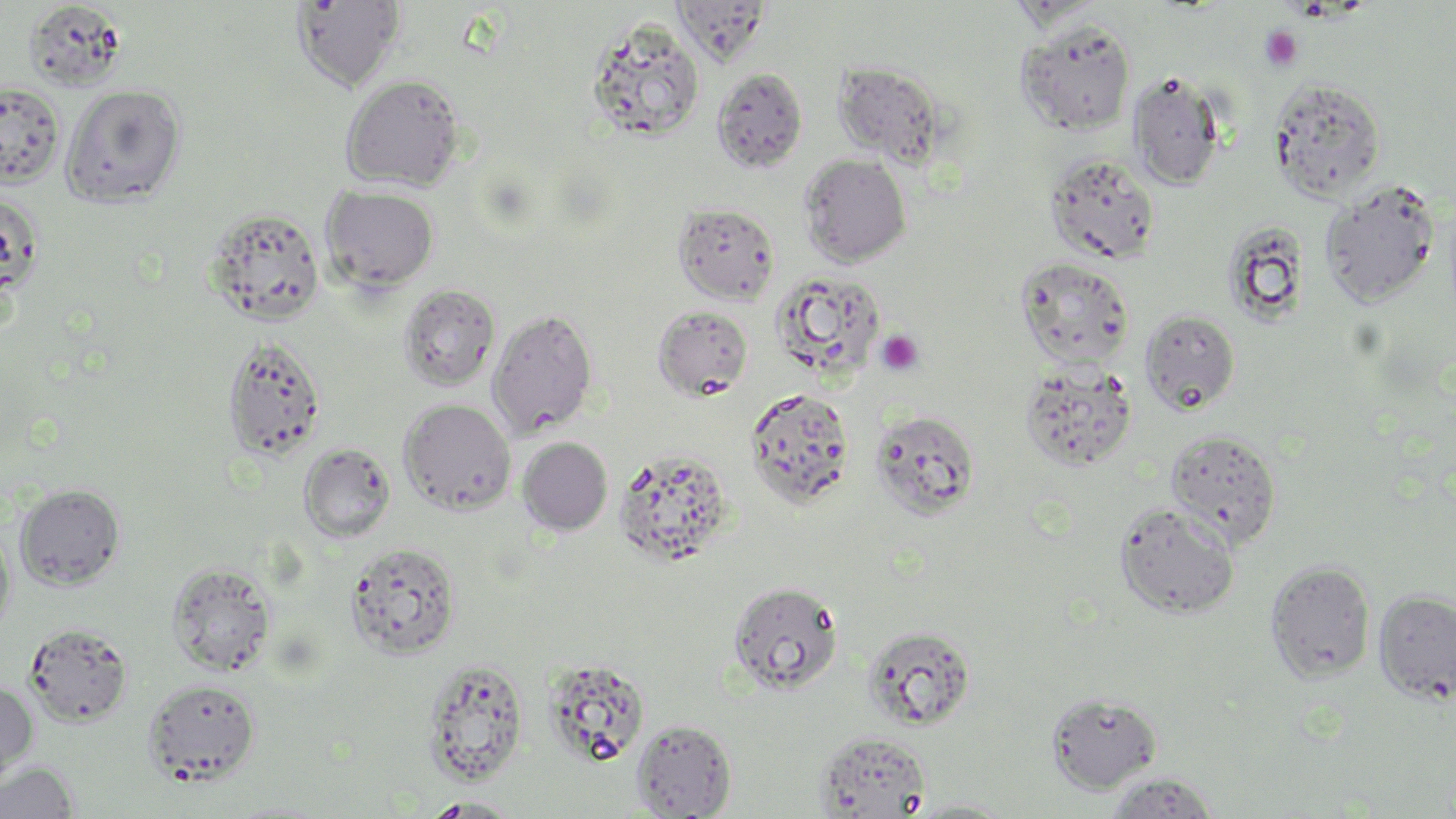
Summary:
  - Coordinate format: approximate bounding boxes as (x1,y1)-(x2,y2) corner pairs in pixels
  - Platelet locations: (1259,25)-(1304,72), (876,329)-(925,376)
  - Uninfected red blood cell locations: (290,0)-(407,93), (672,1)-(771,65), (24,2)-(127,92), (586,18)-(706,142), (1015,18)-(1136,136), (833,62)-(946,166), (711,68)-(807,174), (1128,71)-(1226,190), (340,74)-(466,191), (1269,78)-(1386,202), (0,81)-(65,188), (60,84)-(186,208), (1044,152)-(1160,265), (798,153)-(912,267), (1320,181)-(1440,309), (321,185)-(439,292), (0,191)-(44,304), (672,203)-(780,305), (204,207)-(326,327), (1221,220)-(1311,327), (1015,257)-(1135,370), (770,270)-(887,381), (397,284)-(501,392), (652,305)-(754,401), (487,307)-(598,439), (1139,309)-(1241,416), (222,335)-(327,463), (1020,363)-(1137,472), (745,387)-(854,507), (398,399)-(517,515), (869,409)-(980,520), (1165,429)-(1282,547), (517,437)-(612,535), (298,443)-(396,543), (614,447)-(736,569), (15,484)-(125,590), (1114,501)-(1241,618), (0,522)-(16,642), (346,541)-(462,659), (1265,560)-(1377,683), (167,561)-(277,677), (728,581)-(843,695), (1374,589)-(1456,705), (25,621)-(132,726), (862,625)-(977,730), (542,657)-(650,767), (422,658)-(528,786), (142,678)-(261,786), (0,680)-(37,785), (1045,692)-(1163,793), (631,719)-(736,818), (814,731)-(932,818), (0,761)-(79,819), (1103,772)-(1221,818), (419,796)-(525,817), (906,799)-(1018,817)
  - Slide-level diagnosis: no evidence of blood parasites
  - Preparation: thin blood smear
  - Stain: May-Grünwald-Giemsa
  - Image size: 1456×819 pixels
  - Field of view: one of a larger specimen
  - Magnification: 1000x
  - Modality: optical microscopy